Comment on the morphology of the red blood cells.
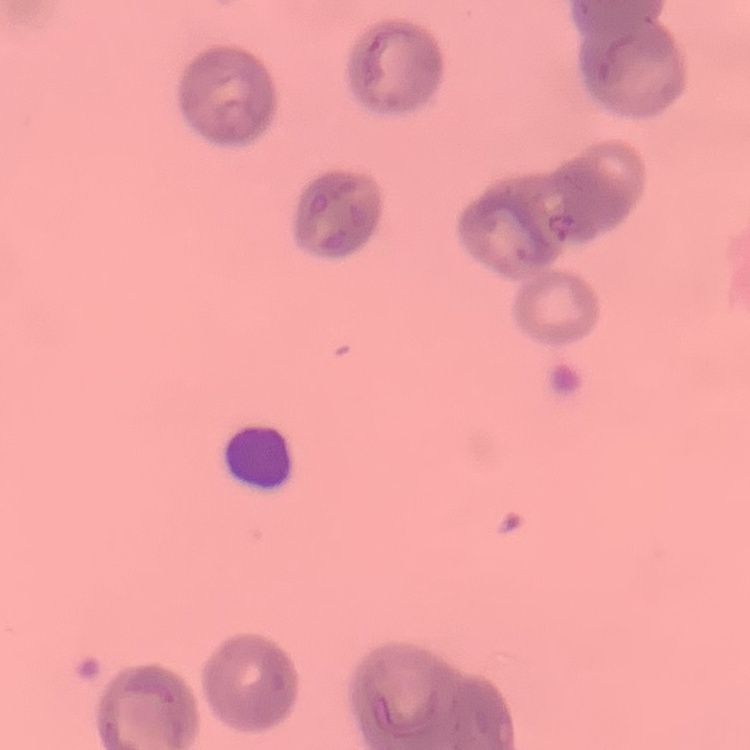
They show rouleaux formation.

Summary:
  - Image type: one tile cut from a larger photomicrograph
  - Preparation: thin blood film
  - Stain: Field's or Giemsa